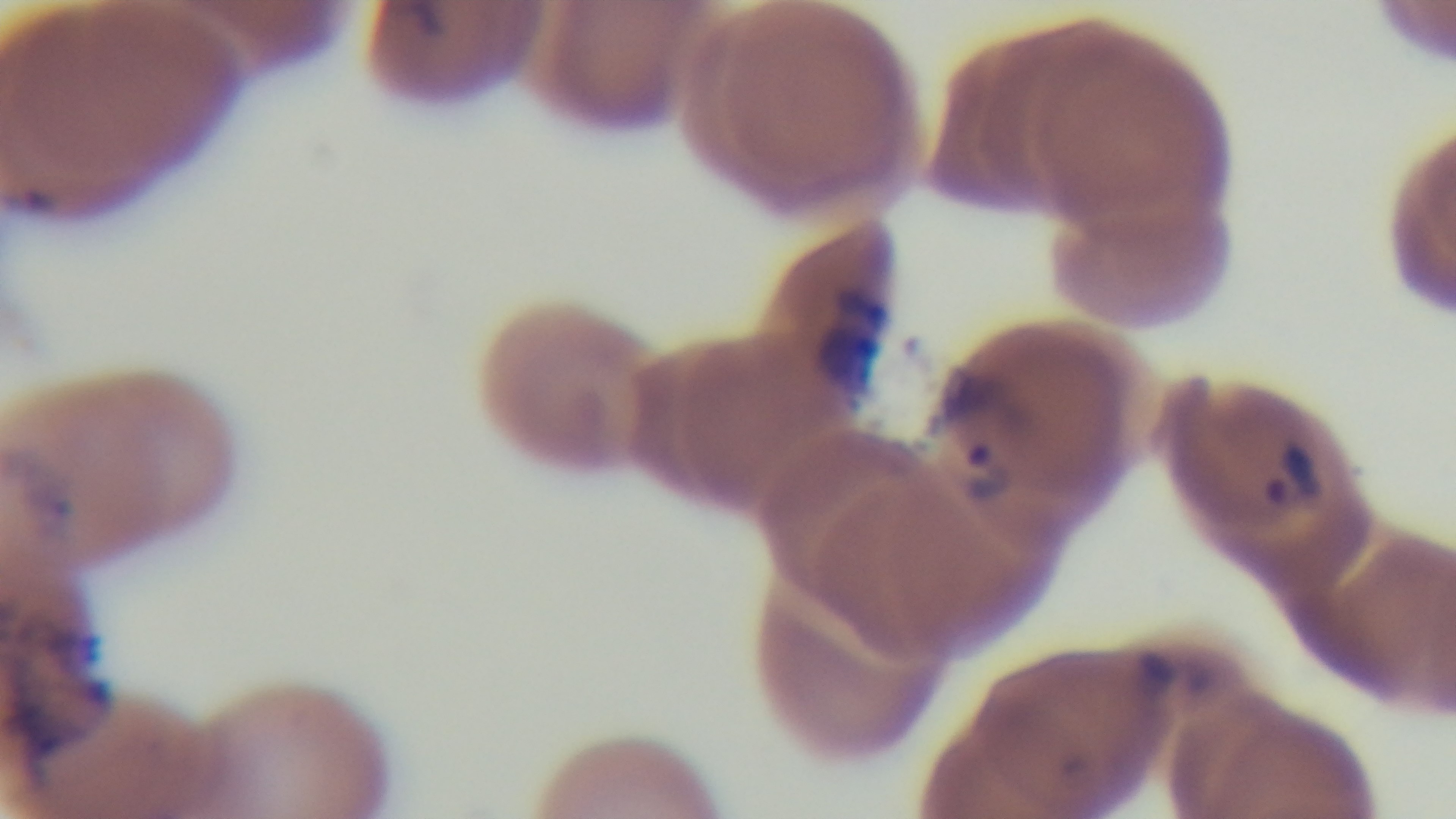

objective: 100x oil immersion
malaria_status: infected
preparation: thin smear
capture: mounted 4K digital camera
stain: Giemsa
field_of_view: one from the slide
modality: light microscopy